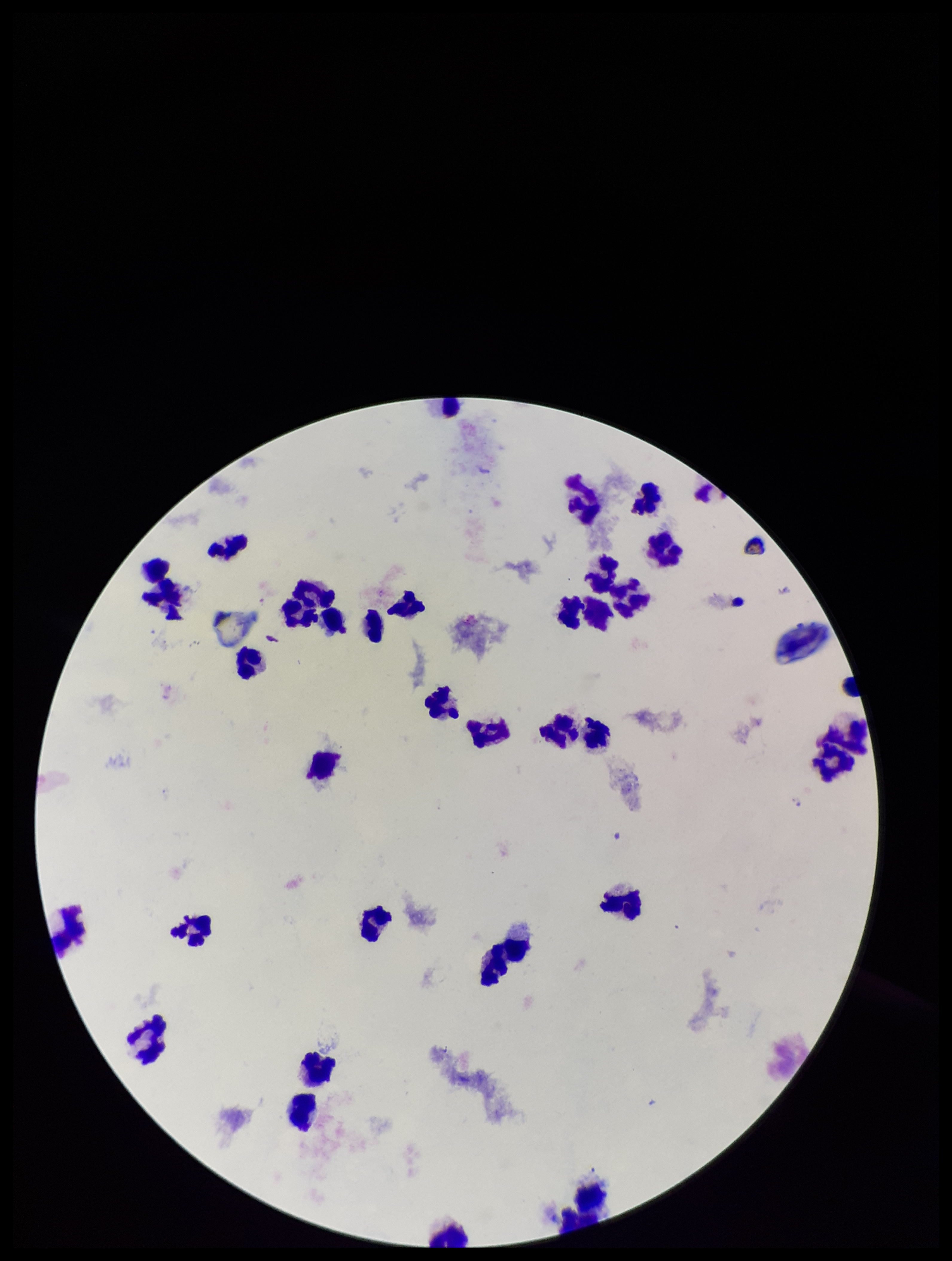 Patient malaria status: negative. Preparation: thick. Leukocyte count: 30. Parasite count: 0. Single field of view. Image is 952×1261 pixels. Plasmodium parasites: none identified. Photographed through the microscope eyepiece with a smartphone camera. Giemsa stain.